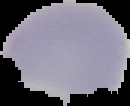

Result: no malaria parasites detected. Image is 130×106 pixels. The area outside the segmented cell region is set to black. From a thin blood film.